Assess this cell for malaria.
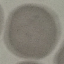

Uninfected.

Summary:
  - Preparation: thin blood smear
  - Image type: cell patch, automatically extracted from a larger field of view and resized to 64 × 64 pixels
  - Capture: smartphone camera at the microscope eyepiece
  - Stain: Giemsa